Comment on the morphology of the red blood cells.
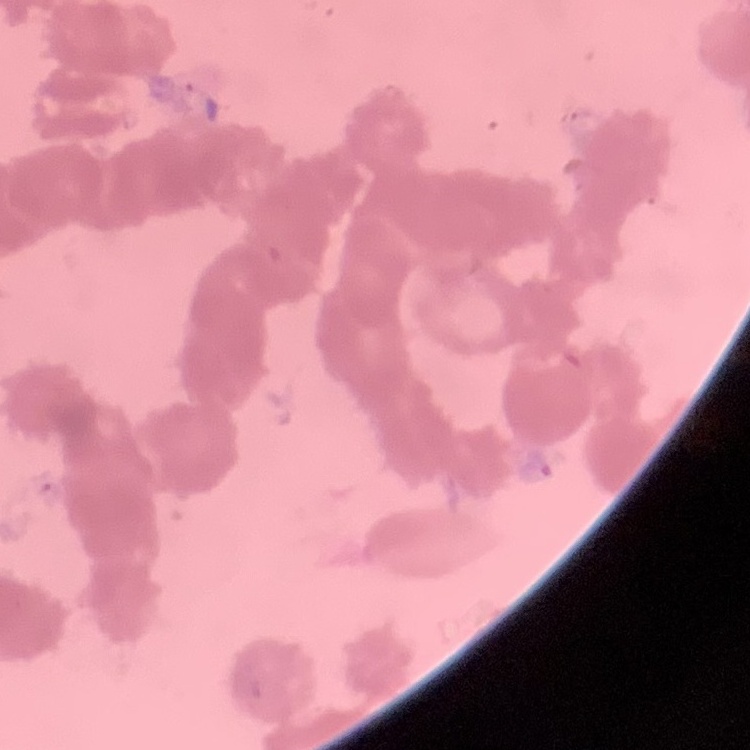
Rouleaux formation.

Field's or Giemsa stain. One tile cut from a larger photomicrograph. Thin blood film.